Locate every blood parasite and identify its species.
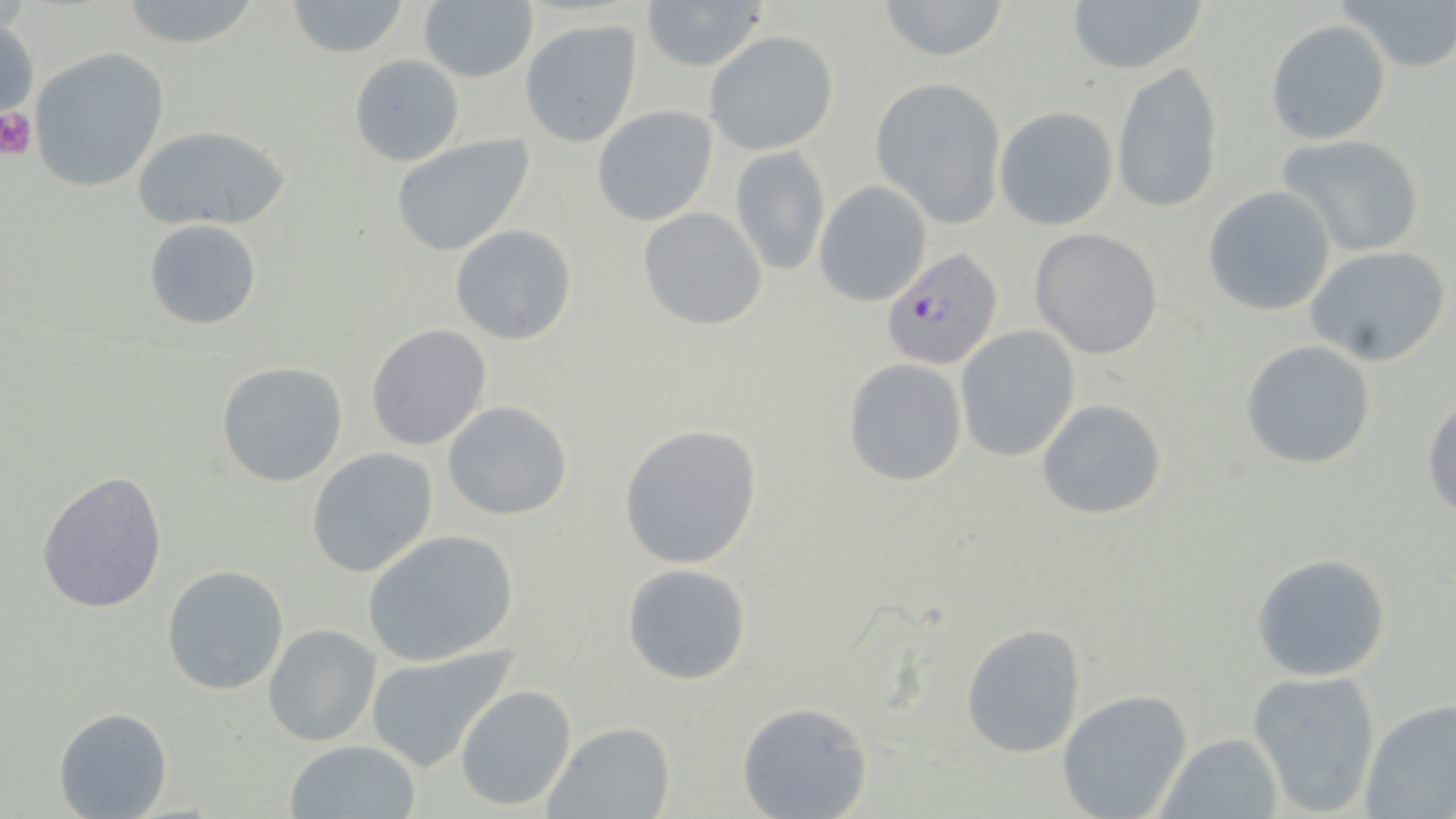
Approximate bounding boxes as (x1, y1, x2, y2) in pixels.
Plasmodium falciparum-infected red blood cells: (882, 247, 1003, 371).
No Plasmodium ovale, Plasmodium malariae, Plasmodium vivax, Babesia divergens, or Trypanosoma brucei observed.

Platelet locations: (0, 107, 38, 159). Uninfected red blood cell locations: (113, 0, 267, 51), (281, 0, 413, 58), (639, 0, 769, 71), (872, 0, 1012, 62), (1065, 0, 1208, 76), (1338, 0, 1456, 74), (418, 2, 539, 84), (0, 15, 39, 129), (1266, 19, 1392, 145), (520, 20, 642, 147), (704, 30, 838, 156), (27, 47, 170, 194), (349, 53, 466, 166), (1111, 61, 1224, 214), (870, 77, 1006, 227), (591, 105, 719, 226), (994, 106, 1119, 230), (132, 125, 291, 232), (1277, 133, 1426, 258), (390, 134, 536, 256), (730, 145, 829, 277), (813, 182, 932, 306), (1201, 185, 1337, 317), (637, 207, 768, 330), (144, 218, 264, 332), (450, 223, 578, 345), (1029, 228, 1165, 360), (1305, 246, 1450, 367), (366, 324, 492, 450), (953, 325, 1081, 463), (1239, 339, 1378, 470), (841, 358, 969, 488), (215, 360, 348, 487), (1422, 392, 1456, 520), (1035, 399, 1169, 520), (441, 400, 573, 521), (618, 421, 764, 570), (306, 449, 439, 578), (37, 470, 168, 615), (363, 529, 521, 667), (1250, 553, 1393, 681), (620, 561, 754, 686), (161, 564, 290, 695), (959, 622, 1090, 758), (263, 624, 382, 747), (366, 646, 516, 774), (1246, 668, 1382, 817), (454, 684, 578, 812), (1056, 689, 1194, 819), (1358, 698, 1456, 819), (736, 701, 873, 819), (54, 707, 173, 819), (544, 722, 677, 819), (1158, 732, 1282, 817), (285, 739, 421, 819). Slide-level diagnosis: Plasmodium falciparum. Light microscopy. May-Grünwald-Giemsa-stained preparation. One field of a larger specimen. Thin blood smear. Captured at 1000x magnification. Image is 1456×819 pixels.